Assess this cell for malaria.
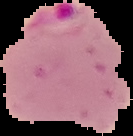

Parasitized.

{
  "preparation": "thin blood smear",
  "image_type": "cell region segmented out of the field of view; surrounding area masked to black",
  "image_size": "133×136 pixels"
}